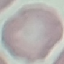

{
  "malaria_status": "uninfected",
  "stain": "Giemsa",
  "capture": "smartphone camera at the microscope eyepiece",
  "preparation": "thin smear",
  "image_type": "automatically extracted cell patch, resized to 64 × 64 pixels"
}